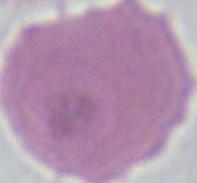

{
  "magnification": "1000x",
  "modality": "photomicrograph",
  "identification": "erythrocyte"
}